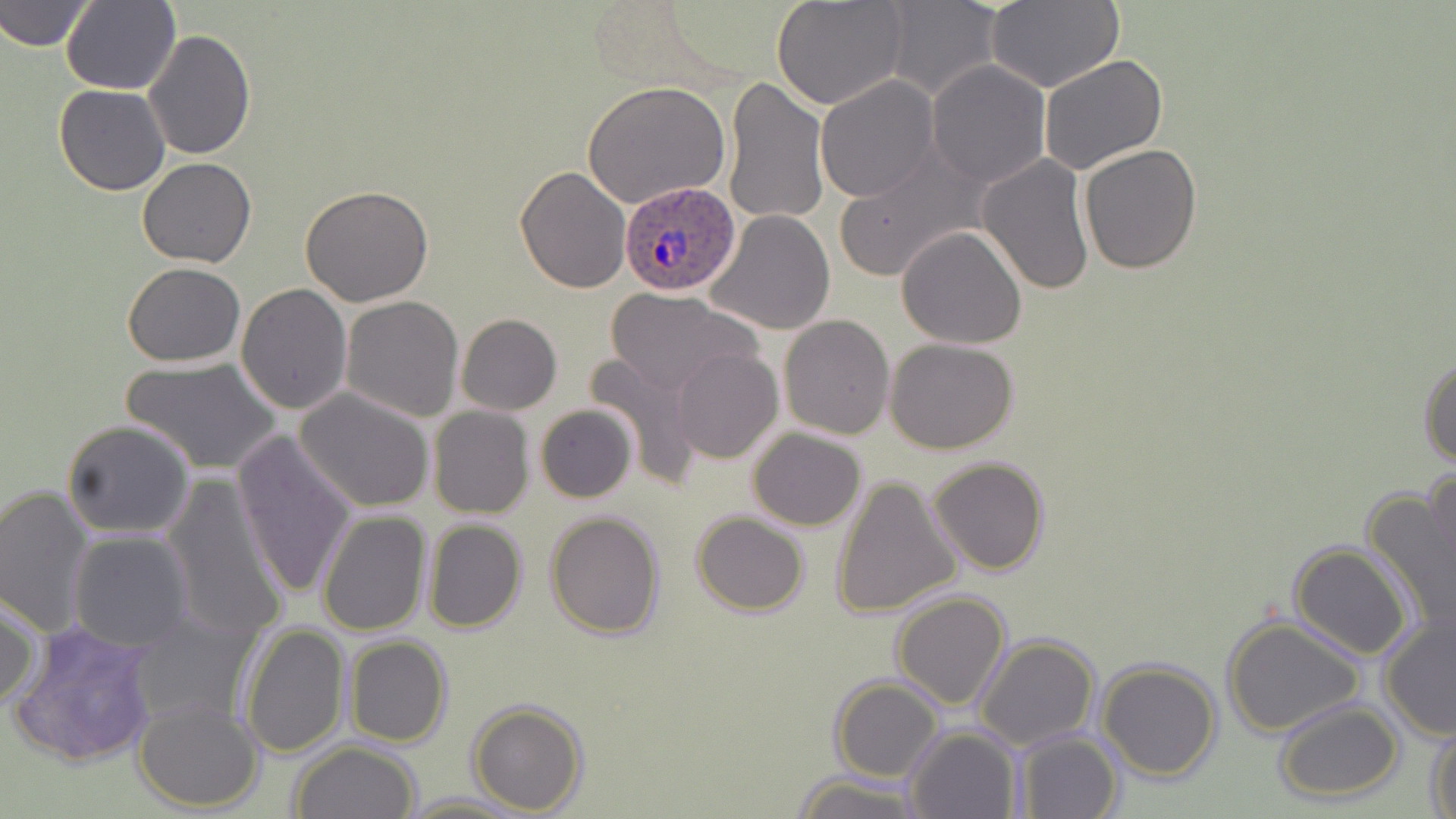

slide-level diagnosis = Plasmodium ovale
modality = optical microscopy
field of view = one of a larger specimen
image size = 1456×819 pixels
preparation = thin blood smear
magnification = 1000x
Plasmodium ovale-infected red blood cell locations = approximate bounding boxes as [x1, y1, x2, y2] in pixels: [619, 182, 742, 296]
uninfected red blood cell locations = approximate bounding boxes as [x1, y1, x2, y2] in pixels: [0, 0, 94, 52], [771, 0, 911, 110], [60, 1, 180, 95], [881, 1, 1002, 101], [982, 3, 1122, 91], [143, 28, 257, 161], [1039, 52, 1168, 175], [926, 61, 1051, 188], [721, 75, 828, 227], [814, 76, 940, 203], [584, 82, 731, 211], [55, 84, 170, 197], [1078, 143, 1203, 274], [833, 146, 988, 284], [976, 154, 1095, 297], [137, 157, 255, 269], [514, 165, 632, 294], [300, 184, 433, 306], [705, 209, 837, 334], [898, 226, 1026, 350], [121, 263, 247, 366], [237, 283, 352, 415], [607, 288, 760, 397], [340, 295, 464, 422], [456, 314, 561, 415], [779, 314, 895, 439], [884, 338, 1019, 455], [672, 349, 783, 464], [584, 353, 704, 481], [1419, 353, 1456, 469], [124, 357, 281, 474], [294, 388, 437, 514], [535, 403, 637, 503], [428, 406, 534, 518], [62, 419, 195, 537], [748, 429, 866, 530], [232, 432, 359, 600], [928, 456, 1051, 575], [1423, 463, 1456, 595], [831, 475, 964, 619], [164, 478, 289, 647], [0, 485, 97, 636], [1364, 488, 1456, 637], [317, 509, 431, 635], [546, 511, 665, 640], [691, 511, 810, 616], [423, 518, 528, 633], [68, 531, 194, 652], [1287, 543, 1416, 660], [891, 590, 1010, 711], [0, 593, 41, 714], [1378, 607, 1456, 741], [129, 608, 260, 730], [1222, 616, 1367, 739], [9, 618, 160, 768], [241, 622, 350, 760], [974, 635, 1099, 751], [344, 636, 452, 748], [1097, 659, 1221, 781], [828, 678, 945, 781], [1273, 698, 1402, 803], [134, 700, 265, 813], [467, 701, 588, 815], [1427, 721, 1456, 819], [905, 725, 1022, 818], [1011, 732, 1123, 819], [290, 741, 423, 819], [792, 771, 921, 819], [404, 792, 525, 818]
stain = May-Grünwald-Giemsa